Name the parasite shown.
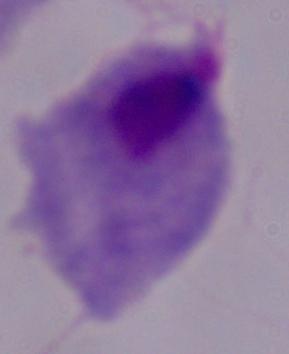
This is a trichomonad.

Captured at 1000x magnification. Micrograph.